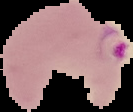
Summary:
  - Result: Plasmodium parasites detected
  - Image size: 133×112 pixels
  - Image type: segmented cell region with the area outside set to black
  - Preparation: thin blood smear